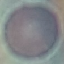
result = negative for malaria parasites
capture = smartphone camera at the microscope eyepiece
preparation = thin blood smear
stain = Giemsa
image type = cell patch, automatically extracted from a larger field of view and resized to 64 × 64 pixels